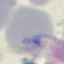
malaria_status: uninfected
preparation: thin smear
stain: Giemsa
capture: smartphone camera at the microscope eyepiece
image_type: cell patch, automatically extracted from a larger field of view and resized to 64 × 64 pixels